Outline each blood parasite and name the species.
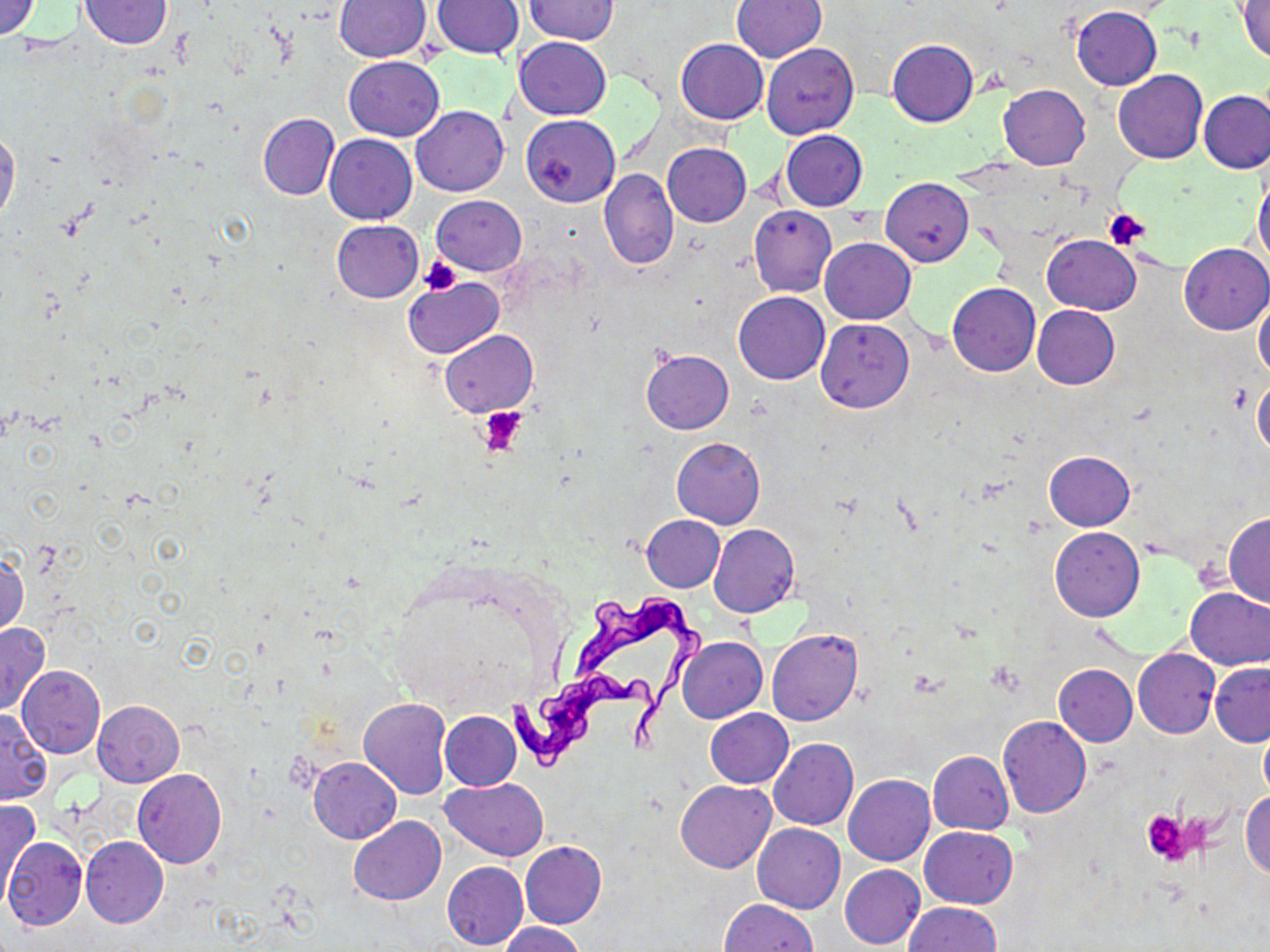
Approximate bounding boxes as (x1, y1, x2, y2) in pixels.
Trypanosoma brucei: (563, 589, 710, 767), (503, 668, 671, 778).
No Plasmodium falciparum, Plasmodium ovale, Plasmodium malariae, Plasmodium vivax, or Babesia divergens observed.

Uninfected red blood cell locations: (0, 0, 42, 41), (733, 0, 828, 62), (78, 1, 172, 49), (335, 1, 431, 61), (431, 1, 523, 61), (525, 1, 618, 44), (1237, 1, 1270, 61), (1070, 5, 1162, 89), (514, 36, 611, 119), (676, 39, 767, 124), (887, 39, 978, 127), (761, 43, 859, 139), (343, 56, 444, 141), (1113, 69, 1207, 163), (998, 84, 1090, 169), (1198, 90, 1270, 175), (411, 106, 509, 196), (257, 114, 339, 199), (521, 115, 619, 206), (0, 127, 21, 225), (780, 130, 868, 211), (325, 134, 417, 224), (662, 143, 751, 226), (600, 168, 678, 269), (1253, 171, 1270, 267), (882, 179, 974, 266), (432, 195, 526, 275), (748, 205, 837, 297), (331, 219, 424, 302), (1044, 234, 1141, 315), (820, 238, 915, 323), (1179, 243, 1270, 334), (404, 276, 503, 358), (947, 283, 1041, 376), (733, 291, 830, 384), (1253, 295, 1270, 379), (1032, 305, 1119, 389), (816, 320, 913, 412), (439, 329, 537, 417), (641, 350, 734, 434), (1252, 377, 1270, 459), (672, 438, 765, 528), (1044, 451, 1134, 531), (1224, 514, 1270, 608), (642, 516, 725, 592), (709, 524, 799, 618), (1049, 527, 1144, 621), (0, 550, 28, 638), (1186, 587, 1269, 669), (0, 622, 49, 716), (766, 629, 862, 726), (677, 637, 767, 723), (1133, 648, 1221, 738), (1210, 661, 1270, 746), (1054, 664, 1137, 746), (18, 667, 104, 758), (358, 698, 452, 800), (93, 700, 185, 787), (1, 707, 53, 803), (706, 707, 792, 787), (441, 711, 520, 789), (997, 716, 1090, 817), (1260, 725, 1270, 800), (769, 738, 858, 830), (928, 751, 1013, 834), (308, 756, 400, 844), (132, 769, 227, 868), (843, 774, 935, 866), (441, 779, 549, 860), (676, 780, 775, 873), (1241, 789, 1270, 878), (1, 797, 39, 903), (348, 816, 446, 904), (752, 823, 845, 913), (919, 826, 1018, 908), (1, 836, 87, 931), (79, 836, 168, 928), (520, 841, 606, 928), (442, 860, 528, 951), (840, 864, 924, 950), (720, 899, 817, 951), (903, 903, 1000, 952), (498, 924, 589, 952). Platelet locations: (1103, 208, 1152, 251), (419, 256, 462, 294), (479, 406, 528, 456), (1142, 809, 1194, 865). Slide-level diagnosis: Trypanosoma brucei. Image is 1270×952 pixels. May-Grünwald-Giemsa-stained preparation. Captured at 1000x magnification. One field of a larger specimen. Light microscopy. Thin blood smear.